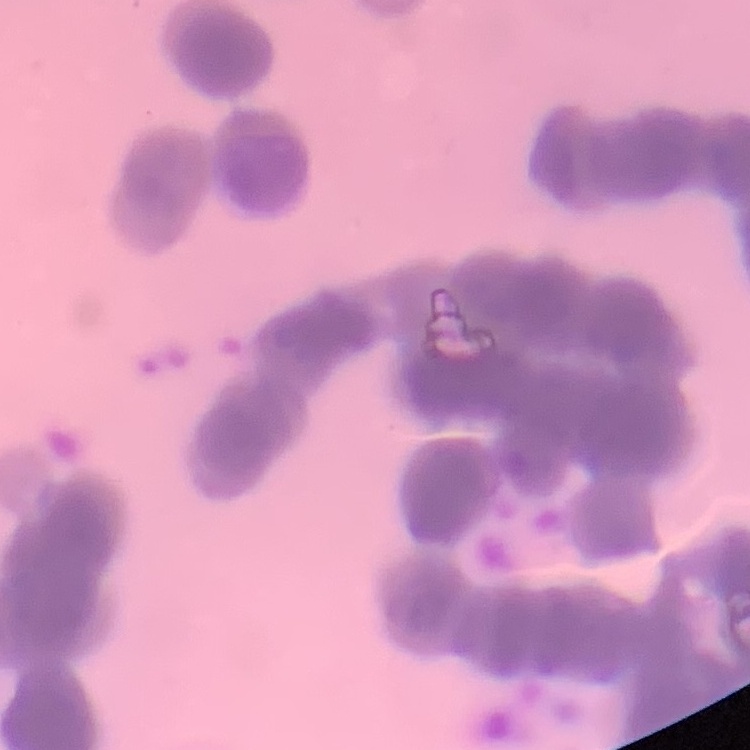

erythrocyte morphology = rouleaux formation
preparation = thin blood smear
stain = Field's or Giemsa
image type = one tile cut from a larger photomicrograph